Outline each Babesia divergens-infected red blood cell.
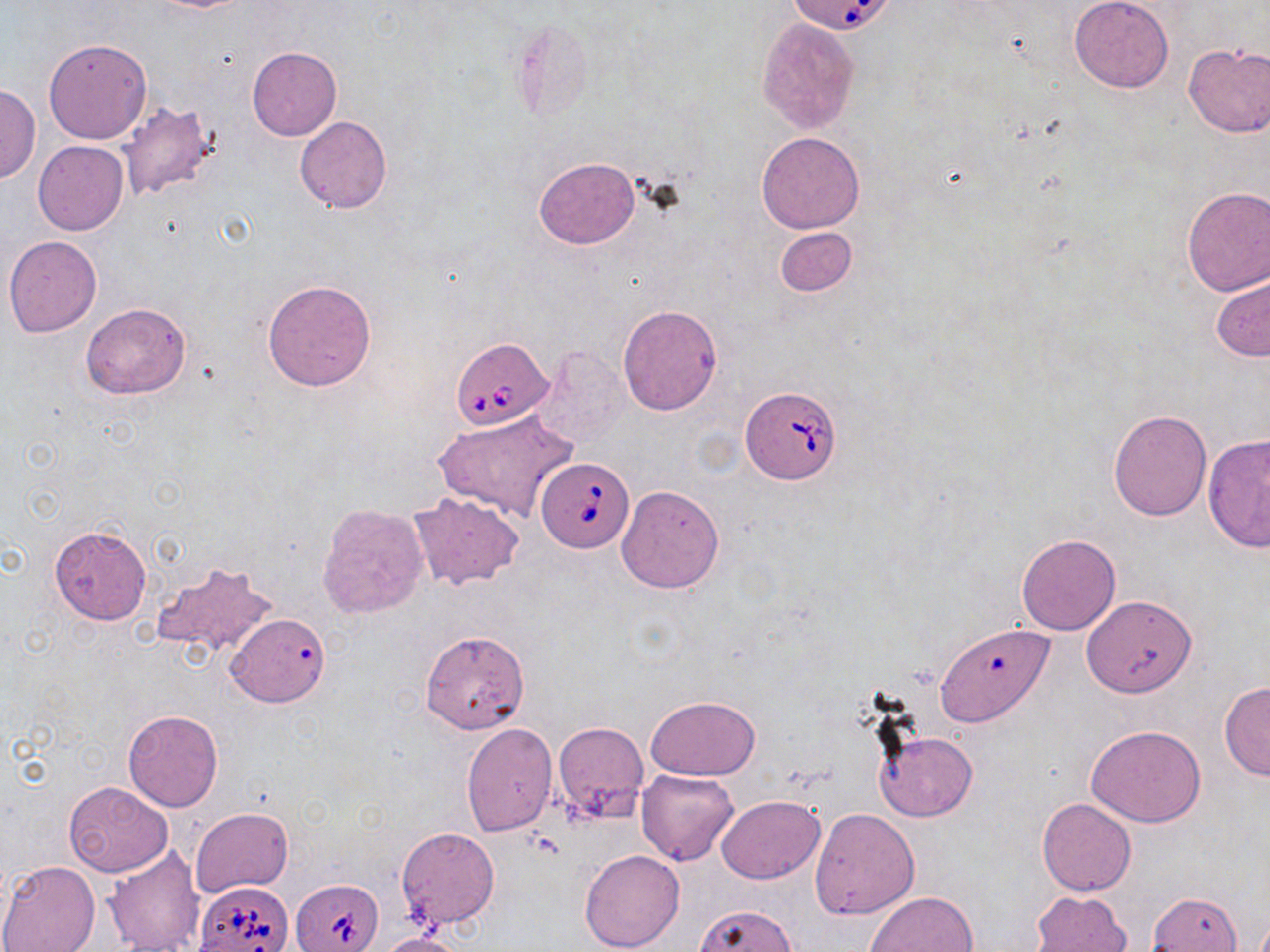
Approximate bounding boxes as (x1,y1)-(x2,y2) corner pairs in pixels.
Babesia divergens-infected red blood cells: (782,0)-(898,35), (450,337)-(554,430), (742,387)-(844,484), (537,457)-(632,552), (292,878)-(383,951), (194,879)-(293,952).

slide-level diagnosis = Babesia divergens
modality = optical microscopy
preparation = thin blood smear
image size = 1270×952 pixels
magnification = 1000x
field of view = one of a larger specimen
stain = May-Grünwald-Giemsa
uninfected red blood cell locations = approximate bounding boxes as (x1,y1)-(x2,y2) corner pairs in pixels: (151,0)-(251,13), (1068,0)-(1174,92), (757,18)-(859,132), (43,38)-(153,145), (1183,43)-(1270,138), (247,46)-(342,141), (0,84)-(40,185), (117,102)-(222,202), (294,116)-(393,213), (757,132)-(866,234), (33,140)-(128,235), (534,156)-(640,249), (1180,186)-(1270,295), (774,226)-(856,296), (4,235)-(102,338), (1212,271)-(1269,362), (262,279)-(376,391), (81,303)-(190,400), (617,303)-(722,415), (528,345)-(633,451), (1108,408)-(1213,522), (435,409)-(577,523), (1202,433)-(1270,553), (616,485)-(724,593), (408,492)-(525,589), (316,503)-(428,619), (49,524)-(152,624), (1016,533)-(1121,636), (150,561)-(277,659), (1082,595)-(1196,697), (227,614)-(330,708), (929,623)-(1055,729), (419,630)-(529,734), (1219,681)-(1270,781), (645,694)-(761,781), (123,710)-(222,811), (552,721)-(648,821), (461,723)-(557,836), (1085,724)-(1207,827), (874,729)-(977,822), (636,769)-(740,866), (64,782)-(172,877), (715,796)-(825,883), (1037,798)-(1136,895), (191,808)-(294,897), (809,808)-(921,919), (396,826)-(500,929), (103,845)-(205,952), (578,850)-(684,952), (0,860)-(100,952), (1030,889)-(1133,952), (865,890)-(978,951), (693,903)-(798,952), (375,931)-(472,952)